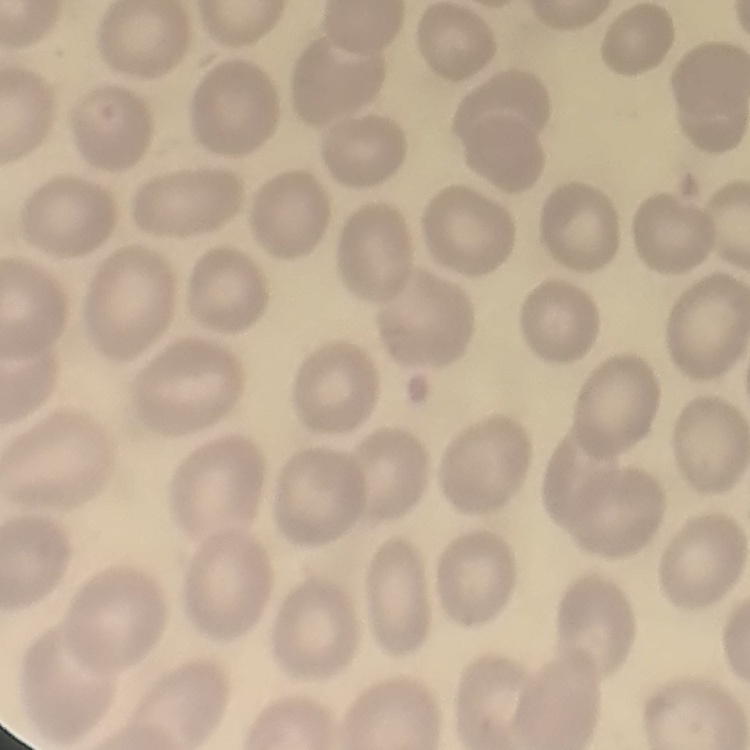

Summary:
  - Erythrocyte morphology: no rouleaux formation
  - Preparation: thin blood smear
  - Image type: square crop of a larger photomicrograph
  - Stain: Field's or Giemsa